Give the preparation type.
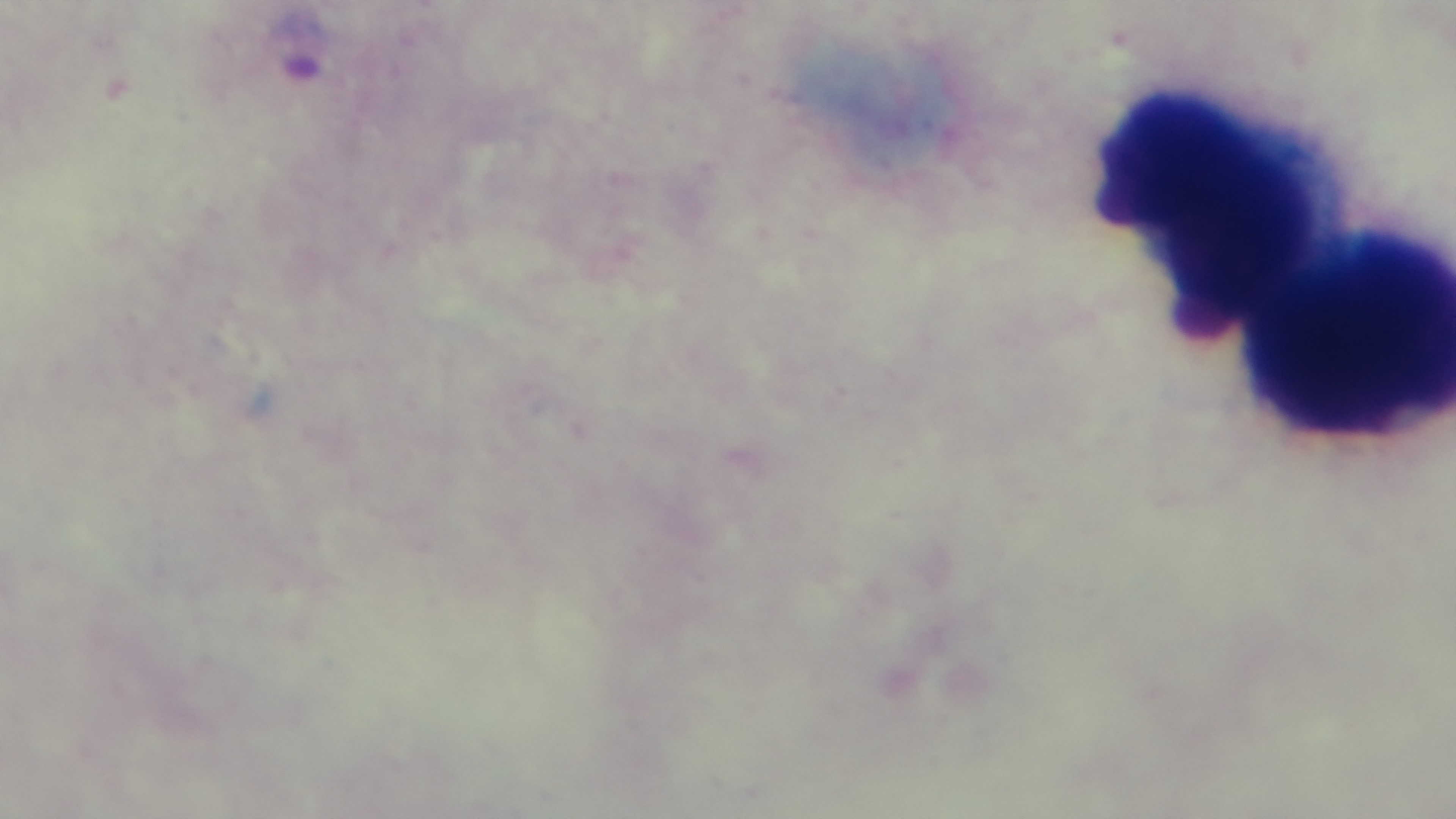
It is a thick blood film.

field_of_view: single
objective: 100x oil immersion
stain: Giemsa
malaria_status: infected
capture: mounted 4K digital camera
modality: light microscopy